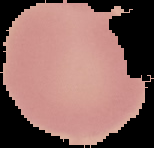
preparation: thin blood smear
image_size: 154×148 pixels
image_type: segmented cell region with the area outside set to black
malaria_status: uninfected